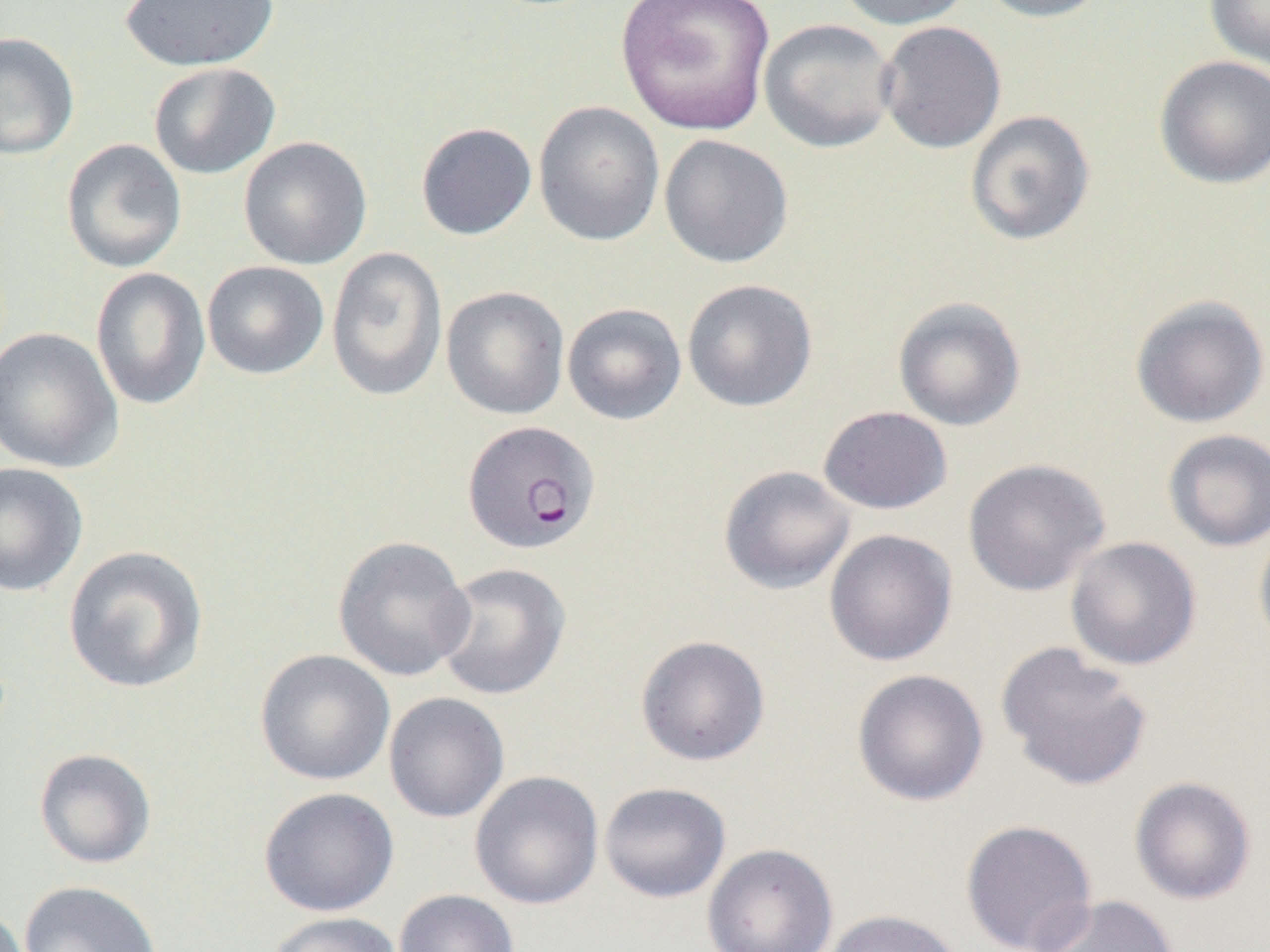

{
  "slide_level_diagnosis": "Plasmodium falciparum",
  "modality": "light microscopy",
  "magnification": "1000x",
  "uninfected_red_blood_cell_locations": "approximate bounding boxes as (x1,y1)-(x2,y2) corner pairs in pixels: (615,0)-(776,136), (831,0)-(974,30), (973,0)-(1111,23), (1204,0)-(1270,69), (118,1)-(279,72), (758,18)-(899,153), (876,21)-(1007,154), (0,31)-(80,160), (1153,55)-(1270,189), (148,62)-(280,180), (533,101)-(665,247), (964,109)-(1096,246), (415,122)-(537,240), (658,134)-(794,268), (238,136)-(372,269), (61,138)-(187,273), (325,246)-(448,401), (202,261)-(329,380), (90,267)-(211,410), (682,278)-(818,412), (440,285)-(570,420), (1129,294)-(1270,428), (892,296)-(1027,432), (561,303)-(687,426), (0,327)-(124,473), (817,405)-(953,515), (1162,428)-(1270,552), (963,458)-(1111,597), (0,461)-(88,596), (718,465)-(856,594), (1253,522)-(1270,658), (824,529)-(958,667), (332,535)-(475,681), (1065,536)-(1202,671), (62,545)-(209,694), (432,562)-(572,700), (635,634)-(771,766), (996,640)-(1153,791), (255,648)-(395,786), (852,668)-(989,806), (383,692)-(510,823), (34,748)-(157,868), (469,770)-(604,910), (1129,776)-(1257,905), (598,782)-(731,903), (258,787)-(399,917), (960,819)-(1098,952), (702,843)-(838,952), (18,880)-(163,952), (394,888)-(519,952), (1027,894)-(1181,952), (820,909)-(966,952), (266,912)-(402,952)",
  "preparation": "thin blood film",
  "image_size": "1270×952 pixels",
  "field_of_view": "one of a larger specimen",
  "plasmodium_falciparum_infected_red_blood_cell_locations": "approximate bounding boxes as (x1,y1)-(x2,y2) corner pairs in pixels: (462,420)-(601,555)"
}